Report the malaria status of this cell.
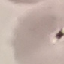
It is uninfected.

Summary:
  - Preparation: thin smear
  - Stain: Giemsa
  - Image type: cell patch, automatically extracted from a larger field of view and resized to 64 × 64 pixels
  - Capture: smartphone camera at the microscope eyepiece